Assess this cell for malaria.
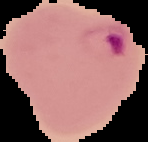
It is parasitized.

Summary:
  - Image type: cell region segmented out of the field of view; surrounding area masked to black
  - Image size: 148×142 pixels
  - Preparation: thin blood smear